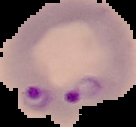

Summary:
  - Image size: 136×127 pixels
  - Malaria status: parasitized
  - Preparation: thin blood film
  - Image type: segmented cell region on a black background